Outline each blood parasite and name the species.
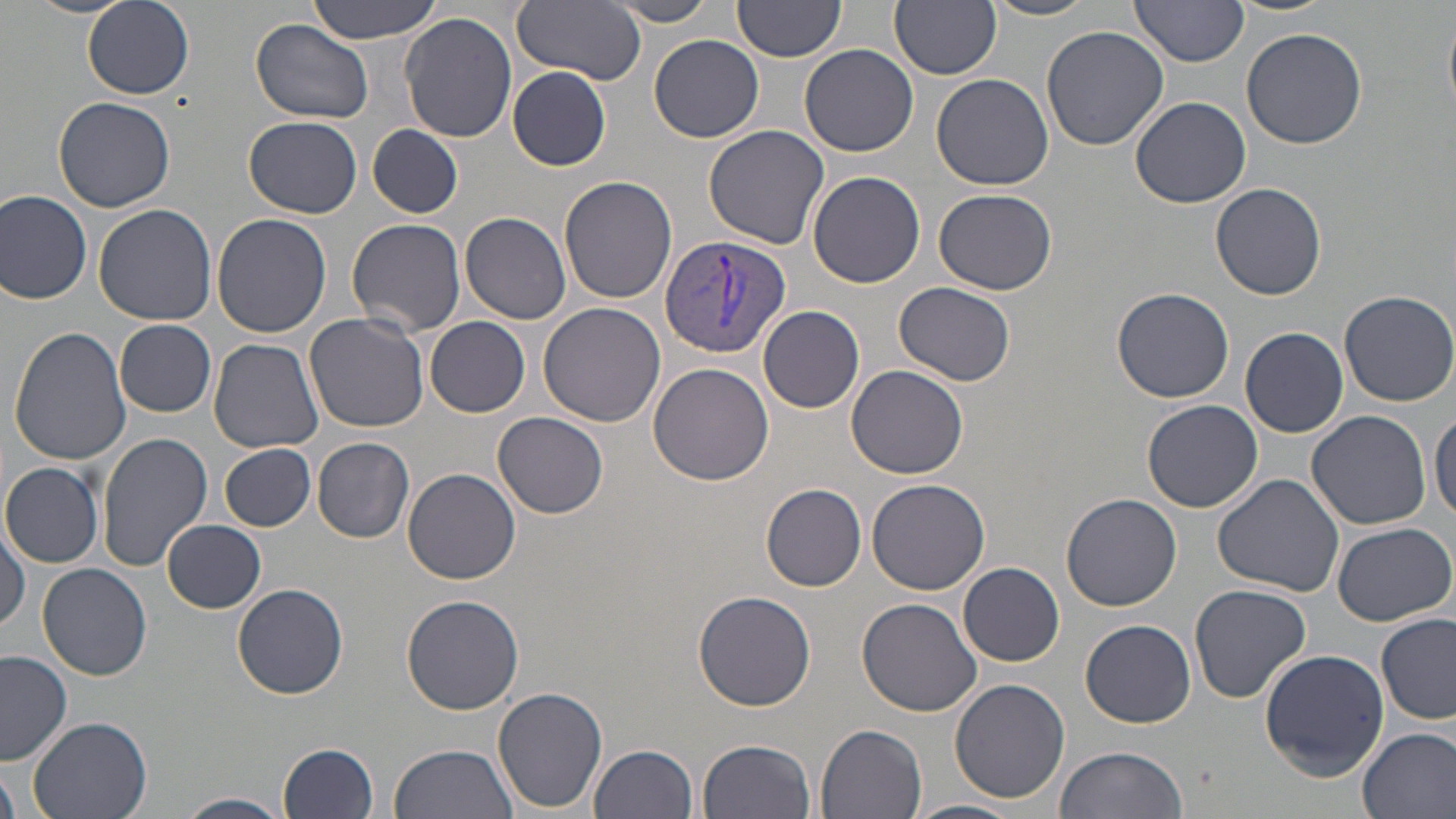

Approximate bounding boxes as named x1/y1/x2/y2 corners in pixels.
Plasmodium vivax-infected red blood cells: (x1=658, y1=232, x2=790, y2=359).
No Plasmodium falciparum, Plasmodium ovale, Plasmodium malariae, Babesia divergens, or Trypanosoma brucei observed.

slide-level diagnosis = Plasmodium vivax
image size = 1456×819 pixels
modality = optical microscopy
magnification = 1000x
field of view = one of a larger specimen
uninfected red blood cell locations = approximate bounding boxes as named x1/y1/x2/y2 corners in pixels: (x1=22, y1=0, x2=139, y2=18), (x1=311, y1=0, x2=443, y2=45), (x1=891, y1=0, x2=1002, y2=79), (x1=1130, y1=0, x2=1250, y2=66), (x1=1228, y1=0, x2=1337, y2=17), (x1=608, y1=1, x2=722, y2=25), (x1=732, y1=1, x2=847, y2=66), (x1=982, y1=1, x2=1103, y2=21), (x1=85, y1=2, x2=194, y2=99), (x1=511, y1=2, x2=647, y2=82), (x1=1443, y1=13, x2=1456, y2=118), (x1=400, y1=14, x2=519, y2=143), (x1=252, y1=17, x2=375, y2=124), (x1=1040, y1=24, x2=1170, y2=151), (x1=1241, y1=26, x2=1366, y2=148), (x1=647, y1=33, x2=764, y2=142), (x1=800, y1=44, x2=918, y2=157), (x1=508, y1=66, x2=611, y2=170), (x1=933, y1=72, x2=1055, y2=190), (x1=53, y1=96, x2=177, y2=211), (x1=1130, y1=96, x2=1251, y2=208), (x1=244, y1=116, x2=364, y2=217), (x1=367, y1=124, x2=462, y2=218), (x1=703, y1=125, x2=831, y2=248), (x1=808, y1=169, x2=925, y2=287), (x1=560, y1=175, x2=678, y2=304), (x1=1211, y1=181, x2=1326, y2=300), (x1=934, y1=188, x2=1058, y2=293), (x1=0, y1=191, x2=93, y2=307), (x1=93, y1=204, x2=218, y2=326), (x1=210, y1=212, x2=332, y2=337), (x1=462, y1=213, x2=571, y2=325), (x1=346, y1=218, x2=469, y2=338), (x1=892, y1=281, x2=1018, y2=387), (x1=1111, y1=287, x2=1235, y2=403), (x1=1339, y1=290, x2=1455, y2=407), (x1=540, y1=303, x2=667, y2=428), (x1=758, y1=304, x2=865, y2=413), (x1=303, y1=314, x2=430, y2=435), (x1=426, y1=315, x2=531, y2=417), (x1=116, y1=320, x2=217, y2=417), (x1=9, y1=326, x2=132, y2=468), (x1=1241, y1=326, x2=1349, y2=437), (x1=208, y1=339, x2=323, y2=455), (x1=649, y1=362, x2=773, y2=485), (x1=846, y1=365, x2=968, y2=479), (x1=1142, y1=401, x2=1263, y2=514), (x1=1431, y1=405, x2=1456, y2=525), (x1=1306, y1=410, x2=1434, y2=530), (x1=494, y1=412, x2=609, y2=519), (x1=95, y1=431, x2=213, y2=572), (x1=313, y1=438, x2=415, y2=543), (x1=220, y1=443, x2=315, y2=531), (x1=1, y1=462, x2=103, y2=566), (x1=404, y1=467, x2=521, y2=584), (x1=1212, y1=472, x2=1346, y2=596), (x1=867, y1=478, x2=990, y2=595), (x1=762, y1=483, x2=867, y2=590), (x1=1061, y1=493, x2=1182, y2=611), (x1=164, y1=519, x2=267, y2=613), (x1=1330, y1=521, x2=1456, y2=625), (x1=0, y1=522, x2=28, y2=631), (x1=958, y1=562, x2=1065, y2=667), (x1=38, y1=564, x2=154, y2=682), (x1=233, y1=582, x2=350, y2=699), (x1=1188, y1=584, x2=1313, y2=702), (x1=693, y1=591, x2=816, y2=712), (x1=402, y1=594, x2=524, y2=714), (x1=856, y1=597, x2=983, y2=717), (x1=1376, y1=614, x2=1455, y2=725), (x1=1080, y1=619, x2=1197, y2=728), (x1=1257, y1=646, x2=1391, y2=779), (x1=0, y1=651, x2=76, y2=766), (x1=949, y1=678, x2=1070, y2=803), (x1=493, y1=686, x2=608, y2=813), (x1=27, y1=716, x2=151, y2=819), (x1=817, y1=724, x2=928, y2=819), (x1=1357, y1=725, x2=1456, y2=819), (x1=698, y1=737, x2=817, y2=819), (x1=278, y1=741, x2=381, y2=819), (x1=589, y1=743, x2=699, y2=819), (x1=389, y1=744, x2=517, y2=819), (x1=1052, y1=746, x2=1191, y2=819), (x1=0, y1=768, x2=20, y2=819), (x1=179, y1=793, x2=290, y2=818), (x1=904, y1=799, x2=1019, y2=819)
stain = May-Grünwald-Giemsa
preparation = thin blood film